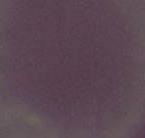
Summary:
  - Magnification: 1000x
  - Modality: photomicrograph
  - Identification: erythrocyte